Describe the morphology of the red blood cells.
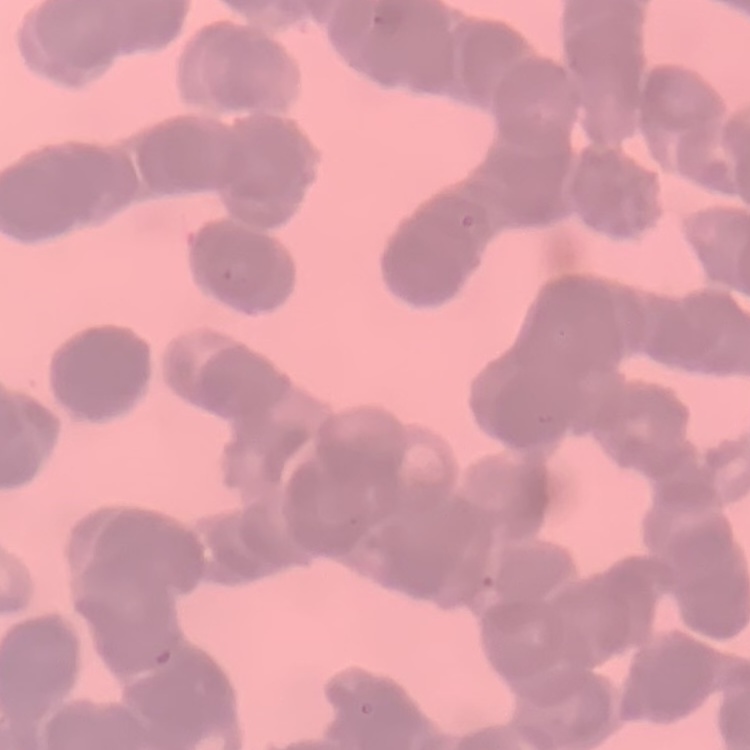

They show rouleaux formation.

stain = Field's or Giemsa
image type = square crop of a larger photomicrograph
preparation = thin blood smear